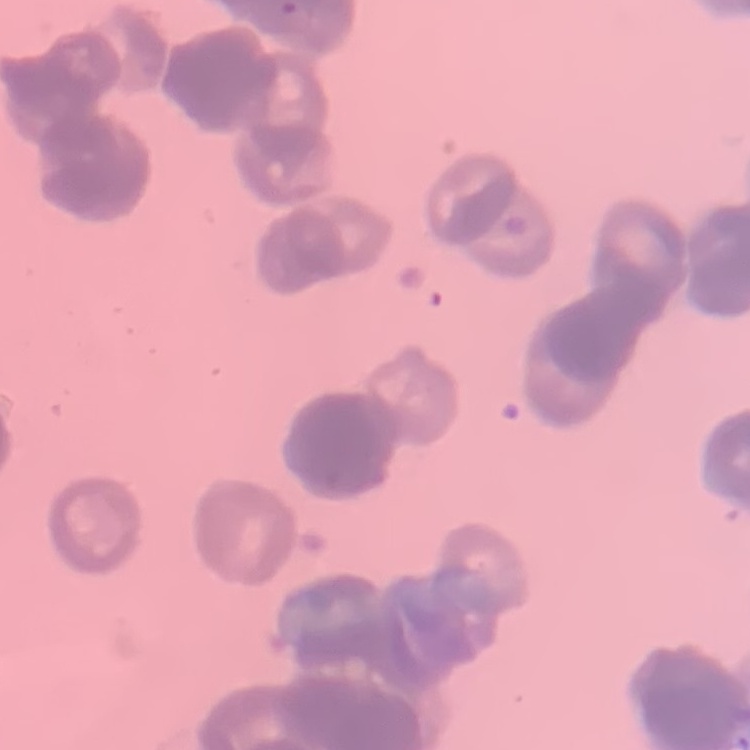

red blood cell morphology = rouleaux formation
stain = Field's or Giemsa
preparation = thin blood film
image type = square crop of a larger photomicrograph